Classify this cell by malaria status.
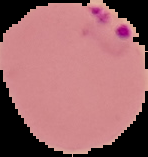

It is parasitized.

preparation: thin blood film
image_size: 148×157 pixels
image_type: segmented cell region on a black background